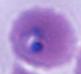

Captured at either 400x or 1000x magnification. Photomicrograph. A Plasmodium parasite is seen.